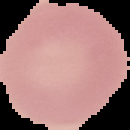

preparation: thin blood smear
result: no malaria parasites seen
image_size: 130×130 pixels
image_type: segmented cell region on a black background